Identify the cell.
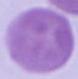
This is an erythrocyte.

Summary:
  - Magnification: 1000x
  - Modality: photomicrograph